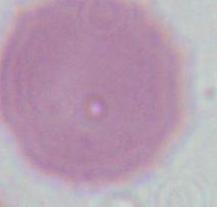
1000x magnification. A red blood cell is seen. Micrograph.